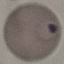
malaria_status: parasitized
preparation: thin blood smear
image_type: cell patch, automatically extracted from a larger field of view and resized to 64 × 64 pixels
capture: smartphone through the microscope eyepiece
stain: Giemsa